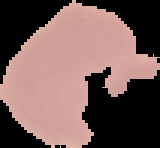

Summary:
  - Image size: 160×148 pixels
  - Preparation: thin blood smear
  - Result: no malaria parasites detected
  - Image type: segmented cell region on a black background